Name the parasite shown.
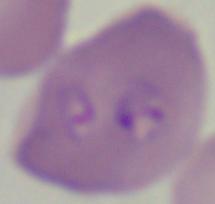

Babesia.

Summary:
  - Magnification: 1000x
  - Modality: photomicrograph